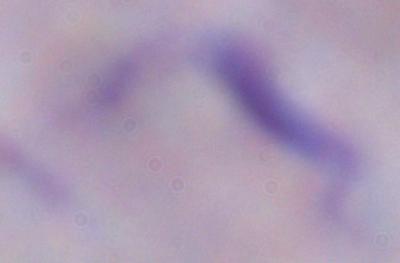
Summary:
  - Magnification: 1000x
  - Modality: photomicrograph
  - Identification: trypanosome